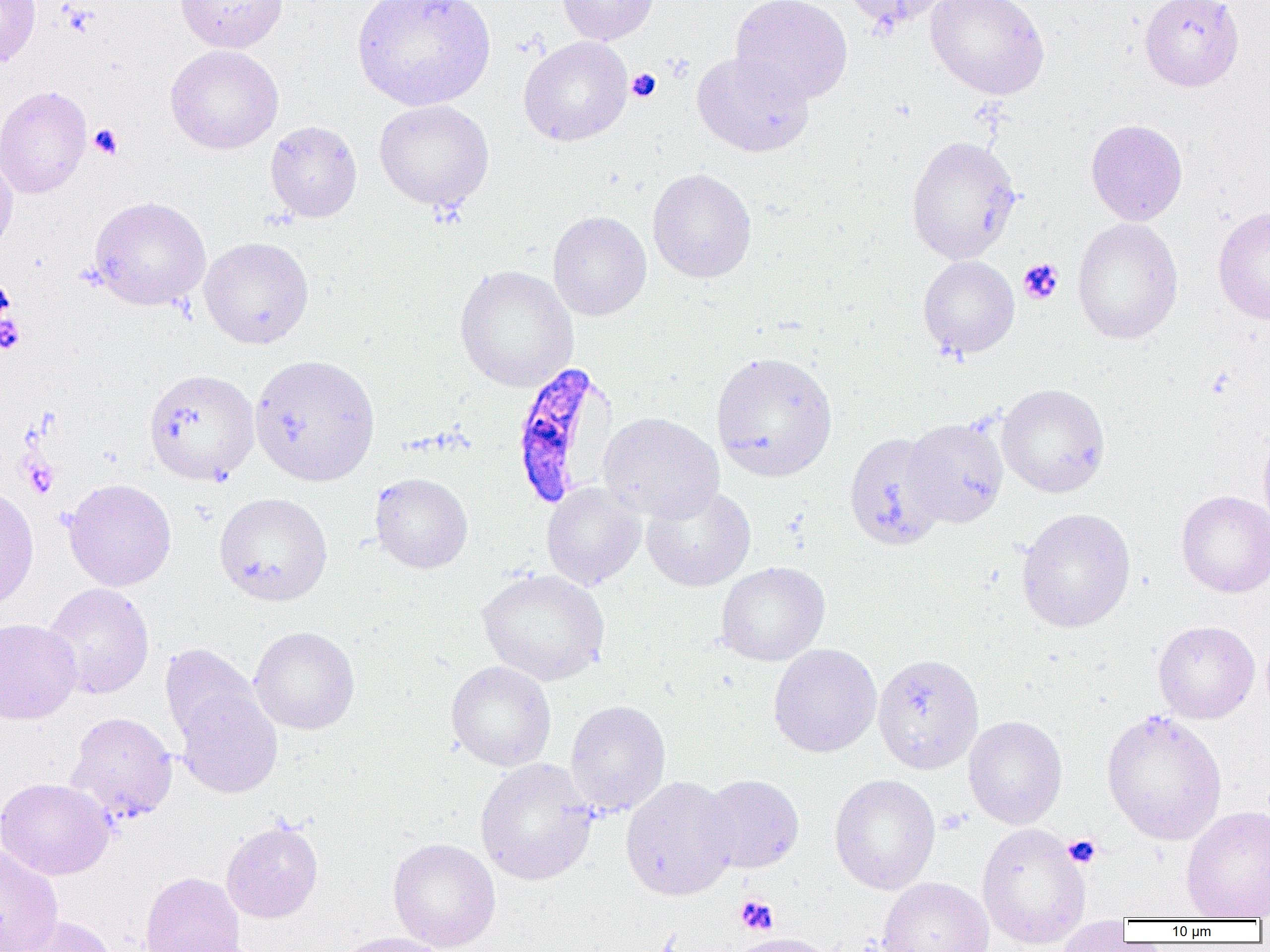

Approximate bounding boxes as named x1/y1/x2/y2 corners in pixels. Plasmodium falciparum-infected red blood cell locations: (x1=509, y1=362, x2=619, y2=509). Platelet locations: (x1=626, y1=69, x2=661, y2=102), (x1=89, y1=123, x2=124, y2=160), (x1=1017, y1=258, x2=1063, y2=305), (x1=0, y1=313, x2=27, y2=354), (x1=23, y1=456, x2=58, y2=497), (x1=938, y1=808, x2=969, y2=834), (x1=1063, y1=834, x2=1101, y2=868), (x1=735, y1=894, x2=778, y2=934). Uninfected red blood cell locations: (x1=0, y1=0, x2=41, y2=67), (x1=175, y1=0, x2=288, y2=53), (x1=352, y1=0, x2=495, y2=110), (x1=557, y1=0, x2=658, y2=45), (x1=730, y1=0, x2=853, y2=105), (x1=845, y1=0, x2=948, y2=31), (x1=925, y1=0, x2=1049, y2=99), (x1=1139, y1=0, x2=1244, y2=92), (x1=518, y1=36, x2=633, y2=146), (x1=165, y1=45, x2=283, y2=153), (x1=692, y1=51, x2=814, y2=158), (x1=0, y1=85, x2=92, y2=199), (x1=374, y1=100, x2=494, y2=211), (x1=1085, y1=119, x2=1188, y2=226), (x1=265, y1=120, x2=362, y2=222), (x1=906, y1=135, x2=1021, y2=264), (x1=0, y1=153, x2=18, y2=261), (x1=647, y1=169, x2=757, y2=283), (x1=88, y1=196, x2=211, y2=311), (x1=1212, y1=206, x2=1270, y2=326), (x1=548, y1=211, x2=652, y2=321), (x1=1072, y1=218, x2=1184, y2=345), (x1=199, y1=237, x2=314, y2=349), (x1=917, y1=255, x2=1019, y2=359), (x1=454, y1=264, x2=579, y2=392), (x1=710, y1=351, x2=838, y2=482), (x1=250, y1=354, x2=380, y2=487), (x1=143, y1=368, x2=260, y2=484), (x1=997, y1=383, x2=1110, y2=497), (x1=598, y1=412, x2=724, y2=523), (x1=903, y1=418, x2=1009, y2=528), (x1=1258, y1=427, x2=1270, y2=535), (x1=844, y1=431, x2=948, y2=552), (x1=370, y1=472, x2=473, y2=574), (x1=62, y1=478, x2=176, y2=591), (x1=542, y1=482, x2=645, y2=590), (x1=641, y1=484, x2=756, y2=592), (x1=0, y1=486, x2=39, y2=609), (x1=1176, y1=490, x2=1270, y2=598), (x1=214, y1=492, x2=333, y2=605), (x1=1016, y1=507, x2=1135, y2=632), (x1=715, y1=561, x2=830, y2=667), (x1=477, y1=568, x2=610, y2=686), (x1=42, y1=583, x2=155, y2=699), (x1=0, y1=618, x2=82, y2=724), (x1=1153, y1=620, x2=1259, y2=724), (x1=249, y1=626, x2=360, y2=735), (x1=769, y1=643, x2=882, y2=757), (x1=159, y1=644, x2=262, y2=747), (x1=872, y1=653, x2=984, y2=774), (x1=445, y1=660, x2=557, y2=771), (x1=175, y1=687, x2=283, y2=799), (x1=565, y1=700, x2=671, y2=816), (x1=1101, y1=709, x2=1227, y2=845), (x1=65, y1=711, x2=178, y2=823), (x1=963, y1=715, x2=1067, y2=829), (x1=475, y1=758, x2=599, y2=886), (x1=698, y1=774, x2=804, y2=873), (x1=829, y1=774, x2=941, y2=894), (x1=620, y1=776, x2=740, y2=901), (x1=1, y1=777, x2=115, y2=880), (x1=1181, y1=805, x2=1270, y2=918), (x1=221, y1=820, x2=323, y2=923), (x1=977, y1=822, x2=1091, y2=949), (x1=388, y1=837, x2=501, y2=952), (x1=0, y1=845, x2=63, y2=952), (x1=139, y1=871, x2=247, y2=952), (x1=876, y1=877, x2=994, y2=952), (x1=11, y1=915, x2=119, y2=952), (x1=1056, y1=917, x2=1133, y2=952), (x1=330, y1=931, x2=453, y2=952), (x1=726, y1=932, x2=836, y2=952). Slide-level diagnosis: Plasmodium falciparum. 1000x magnification. Optical microscopy. Thin blood smear. Image is 1270×952 pixels. Single field of view.